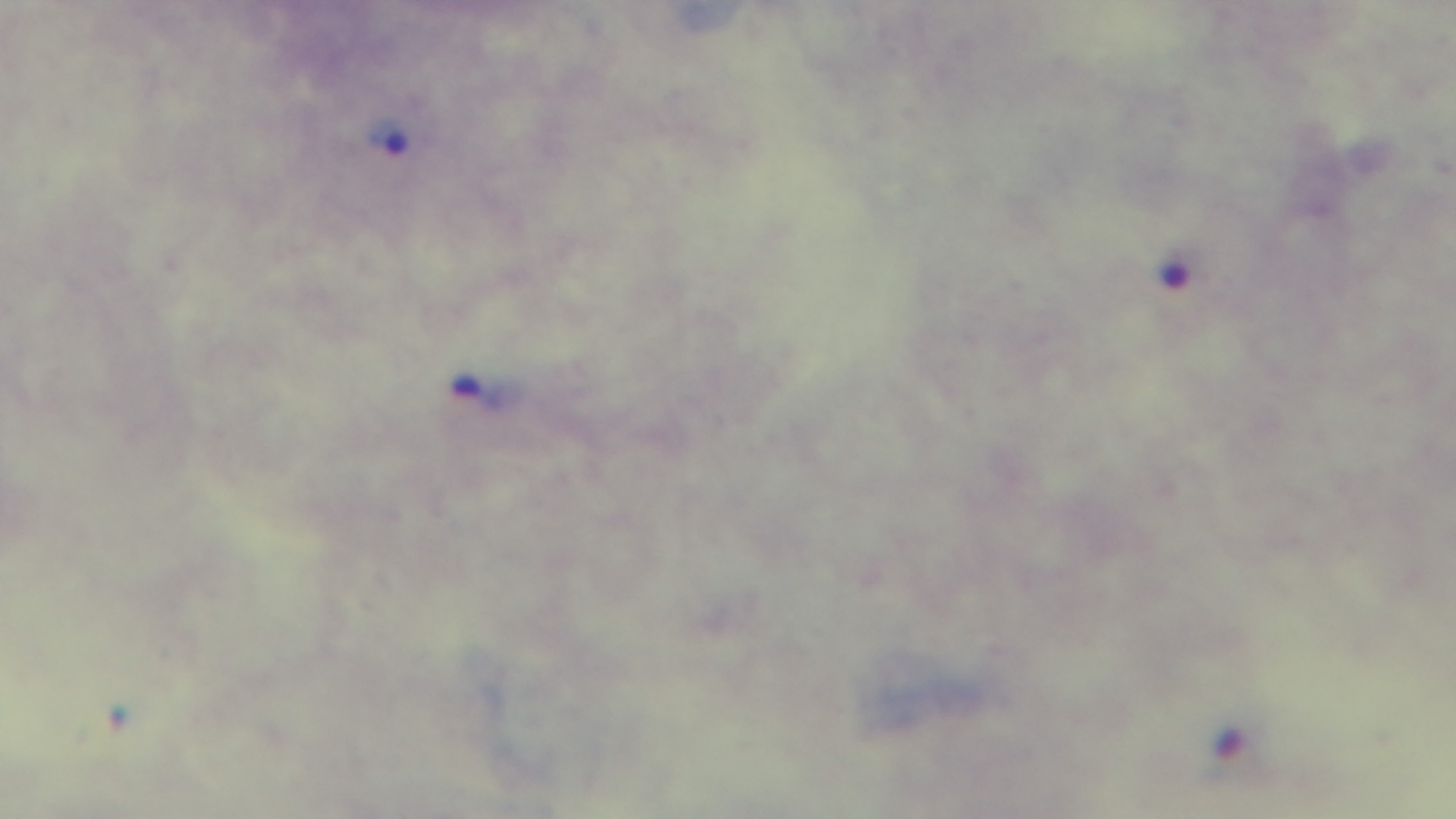

Summary:
  - Field of view: single
  - Capture: mounted 4K digital camera
  - Malaria status: infected
  - Objective: 100x oil immersion
  - Stain: Giemsa
  - Preparation: thick blood film
  - Modality: light microscopy